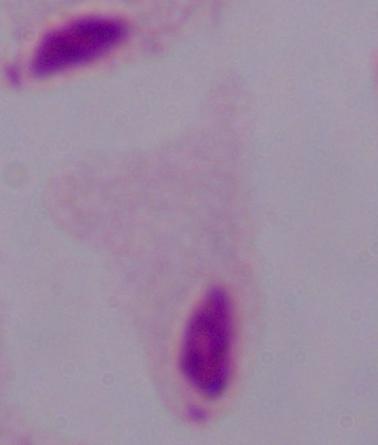 A trichomonad is shown. Captured at 1000x magnification. Micrograph.